Assess this cell for malaria.
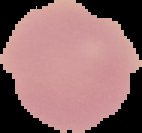
Uninfected.

Summary:
  - Image type: segmented cell region with the area outside set to black
  - Preparation: thin blood film
  - Image size: 142×133 pixels